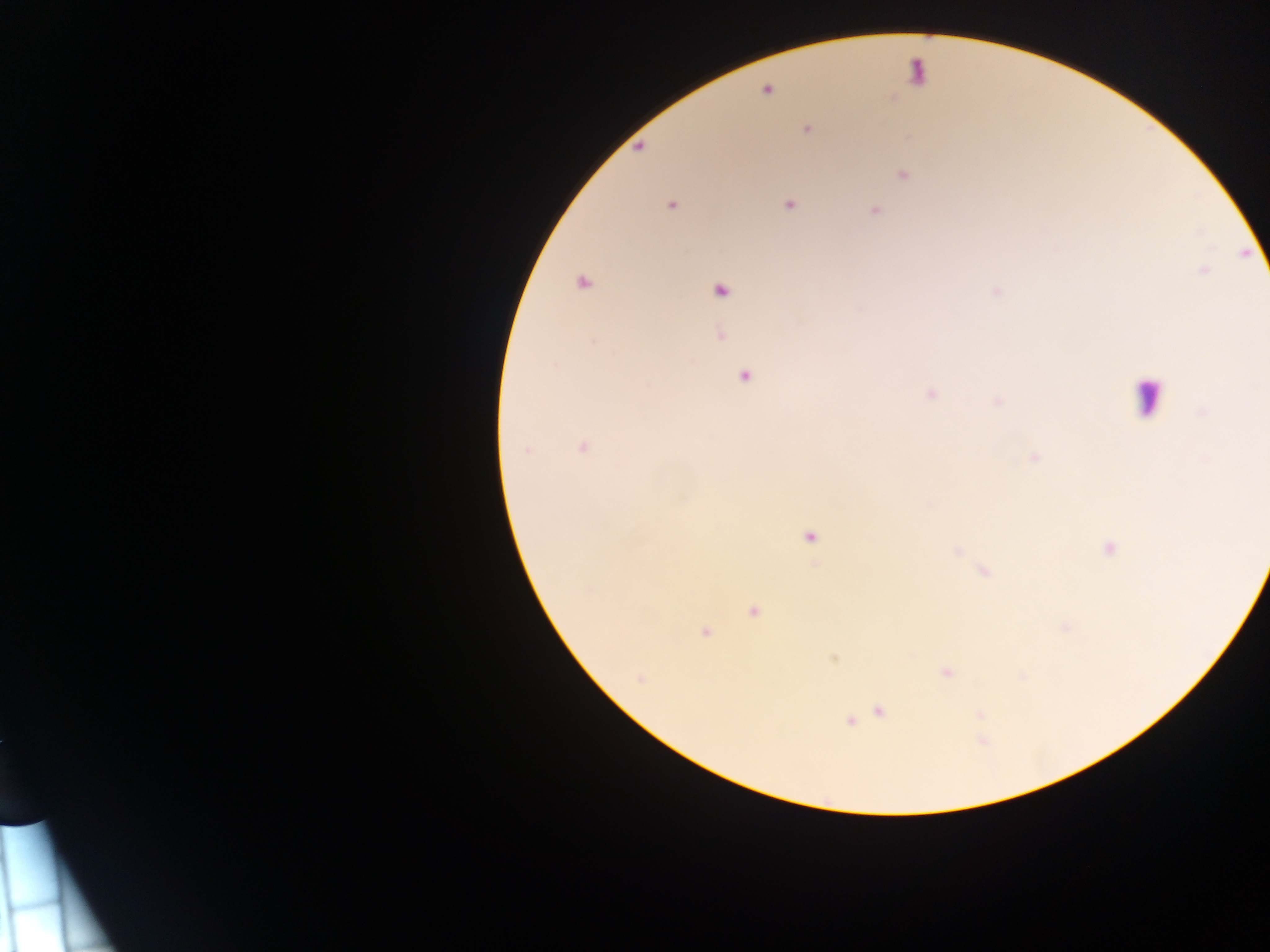

Approximate centers as {x, y} in pixels. Plasmodium parasite locations: {767, 90}, {807, 130}, {903, 175}, {789, 205}, {671, 206}, {875, 211}, {583, 282}, {720, 290}, {594, 341}, {744, 376}, {931, 394}, {1203, 412}, {583, 447}, {525, 451}, {1035, 458}, {809, 537}, {1109, 549}, {753, 611}, {1066, 627}, {705, 632}, {947, 673}, {640, 679}, {879, 711}, {849, 722}. Leukocyte locations: {1148, 395}. Single field of view. Mobile-phone photograph taken through the microscope. Sample from Ghana. Image is 1270×952 pixels. Thick blood smear.